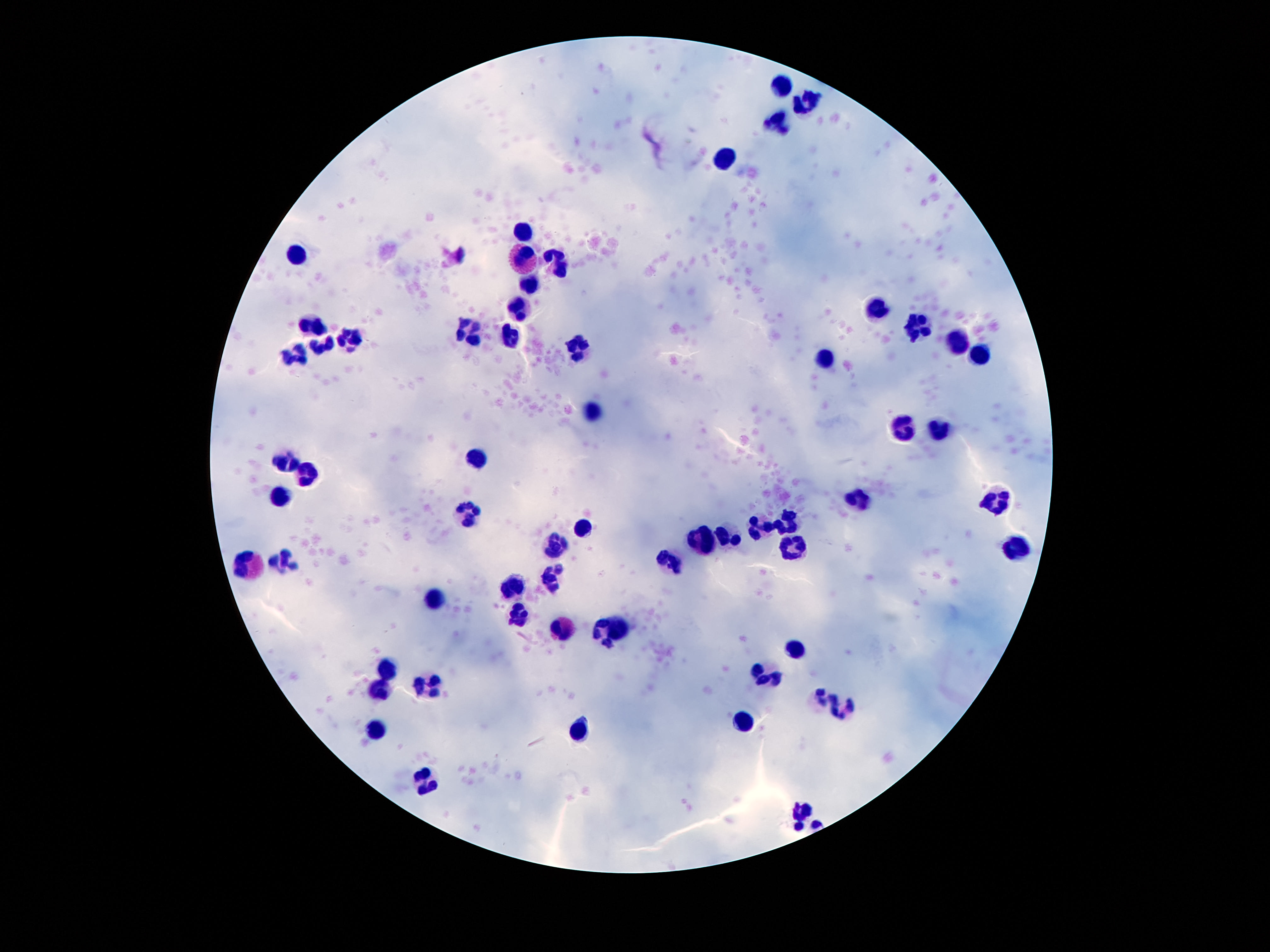

Approximate centers as (x, y) in pixels. Leukocyte locations: (781, 82), (810, 97), (774, 119), (726, 157), (523, 229), (300, 252), (522, 259), (556, 262), (529, 281), (878, 306), (518, 308), (311, 321), (918, 325), (468, 330), (507, 332), (349, 336), (322, 342), (959, 342), (575, 346), (980, 353), (296, 354), (824, 356), (590, 408), (904, 424), (937, 426), (474, 457), (284, 458), (309, 473), (282, 495), (859, 500), (1000, 503), (466, 512), (788, 520), (585, 525), (761, 527), (729, 536), (702, 538), (558, 544), (789, 546), (1015, 548), (672, 555), (287, 559), (249, 566), (553, 574), (515, 585), (438, 596), (517, 610), (560, 625), (618, 628), (598, 632), (797, 650), (384, 666), (764, 675), (431, 683), (376, 685), (820, 696), (842, 710), (737, 718), (374, 726), (579, 729), (425, 780), (801, 810). Thick peripheral-blood smear. Patient malaria status: uninfected. Single field of view. Giemsa stain. 100x magnification. Photographed through the microscope eyepiece with a smartphone camera. Image is 1270×952 pixels.